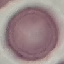
malaria status = uninfected
capture = smartphone camera at the microscope eyepiece
image type = cell patch, automatically extracted from a larger field of view and resized to 64 × 64 pixels
stain = Giemsa
preparation = thin smear